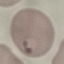

result = malaria parasites detected
capture = smartphone camera at the microscope eyepiece
image type = automatically extracted cell patch, resized to 64 × 64 pixels
stain = Giemsa
preparation = thin smear